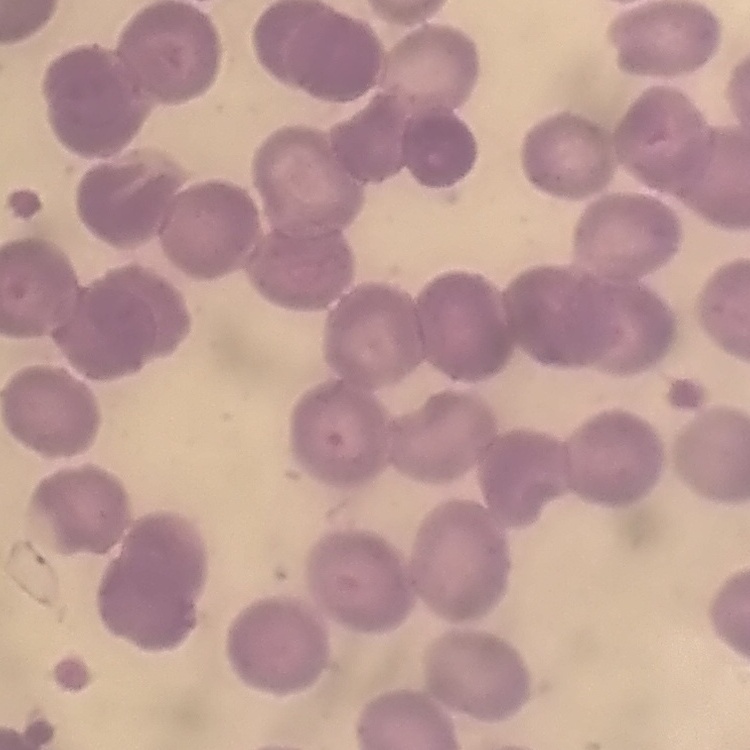
The red blood cells show no rouleaux formation. Field's or Giemsa stain. Thin blood smear. Square crop of a larger photomicrograph.